Identify the blood parasite species.
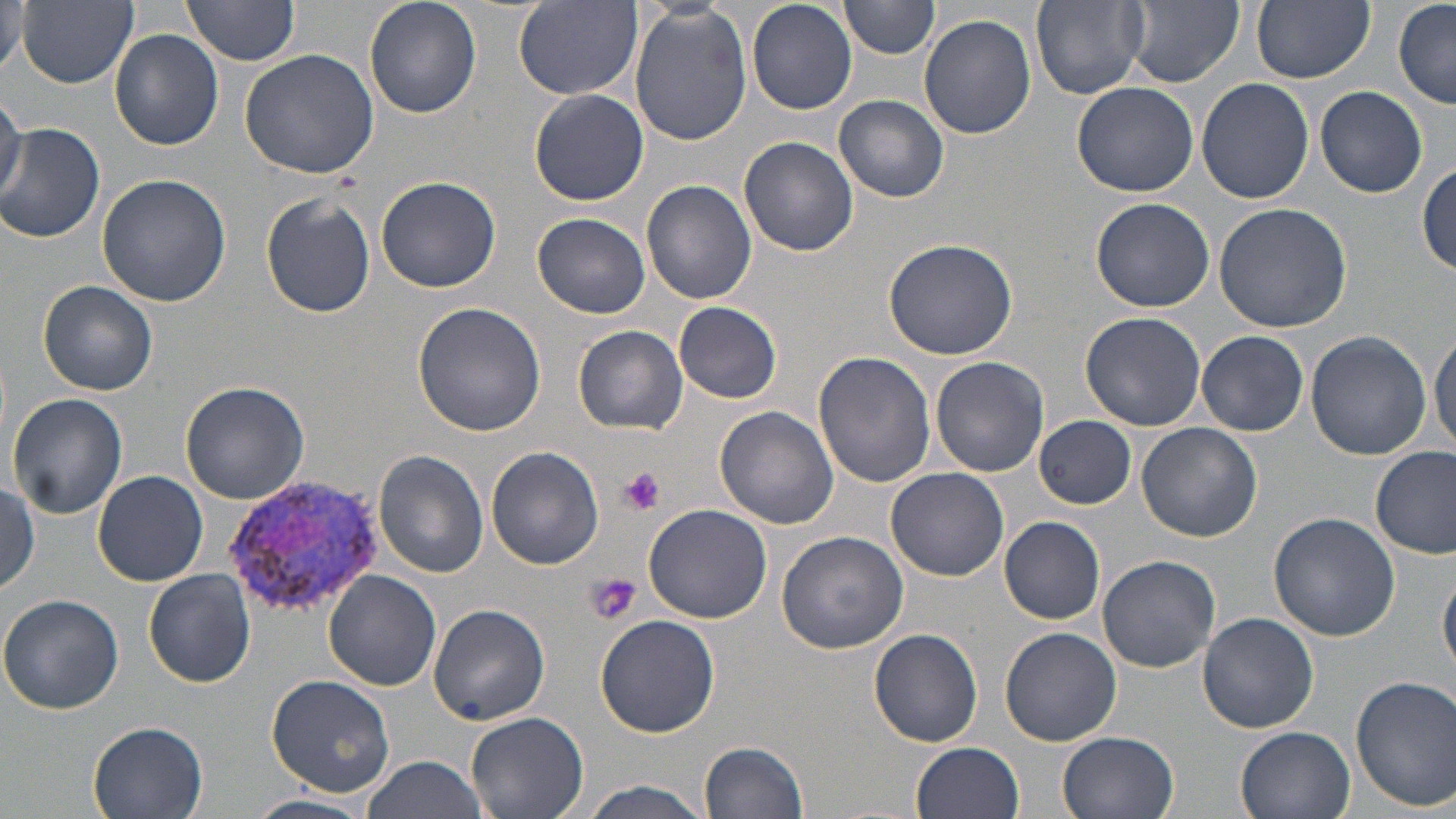
Plasmodium vivax.

uninfected red blood cell locations = approximate bounding boxes as [x1, y1, x2, y2] in pixels: [181, 0, 302, 65], [514, 0, 641, 101], [747, 0, 858, 115], [839, 0, 939, 58], [1032, 0, 1150, 100], [1127, 0, 1243, 88], [17, 1, 138, 88], [366, 1, 482, 117], [1251, 1, 1374, 84], [1, 3, 32, 76], [627, 3, 753, 148], [1395, 3, 1455, 108], [919, 14, 1036, 140], [111, 28, 224, 150], [239, 48, 378, 178], [1196, 78, 1315, 205], [1072, 82, 1201, 198], [1315, 85, 1428, 198], [529, 89, 649, 206], [0, 93, 26, 212], [835, 95, 951, 203], [0, 122, 105, 244], [739, 135, 858, 257], [1416, 162, 1455, 275], [97, 173, 231, 307], [376, 174, 502, 293], [642, 178, 757, 305], [260, 190, 376, 317], [1090, 196, 1214, 312], [1213, 203, 1352, 332], [531, 212, 651, 319], [883, 238, 1018, 360], [38, 280, 159, 397], [413, 301, 550, 435], [675, 301, 781, 403], [1079, 312, 1206, 430], [573, 325, 687, 434], [1430, 328, 1456, 455], [1196, 329, 1308, 436], [1305, 331, 1432, 460], [813, 350, 937, 488], [930, 356, 1050, 477], [180, 378, 310, 504], [7, 392, 127, 518], [713, 406, 840, 531], [1034, 415, 1135, 509], [1136, 422, 1263, 542], [1372, 445, 1455, 559], [485, 446, 604, 571], [373, 450, 489, 577], [885, 466, 1009, 581], [92, 470, 209, 585], [1, 479, 41, 592], [642, 502, 772, 624], [1268, 513, 1400, 642], [999, 515, 1105, 624], [776, 529, 909, 654], [1097, 554, 1220, 673], [1439, 564, 1456, 675], [144, 569, 256, 687], [325, 570, 440, 690], [0, 594, 125, 715], [428, 605, 549, 725], [1197, 611, 1321, 733], [595, 613, 722, 738], [999, 627, 1123, 748], [868, 629, 984, 748], [1351, 674, 1456, 812], [265, 675, 395, 795], [465, 710, 590, 819], [86, 722, 209, 818], [1235, 726, 1357, 819], [1058, 731, 1181, 819], [700, 739, 810, 818], [913, 741, 1025, 819], [361, 755, 489, 819], [575, 779, 718, 819], [246, 794, 381, 819]
preparation = thin blood film
Plasmodium vivax-infected red blood cell locations = approximate bounding boxes as [x1, y1, x2, y2] in pixels: [221, 473, 387, 619]
image size = 1456×819 pixels
platelet locations = approximate bounding boxes as [x1, y1, x2, y2] in pixels: [616, 466, 665, 515], [584, 573, 642, 626]
modality = light microscopy
field of view = one of a larger specimen
magnification = 1000x
stain = May-Grünwald-Giemsa